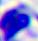
Summary:
  - Modality: micrograph
  - Magnification: 400x
  - Identification: leukocyte